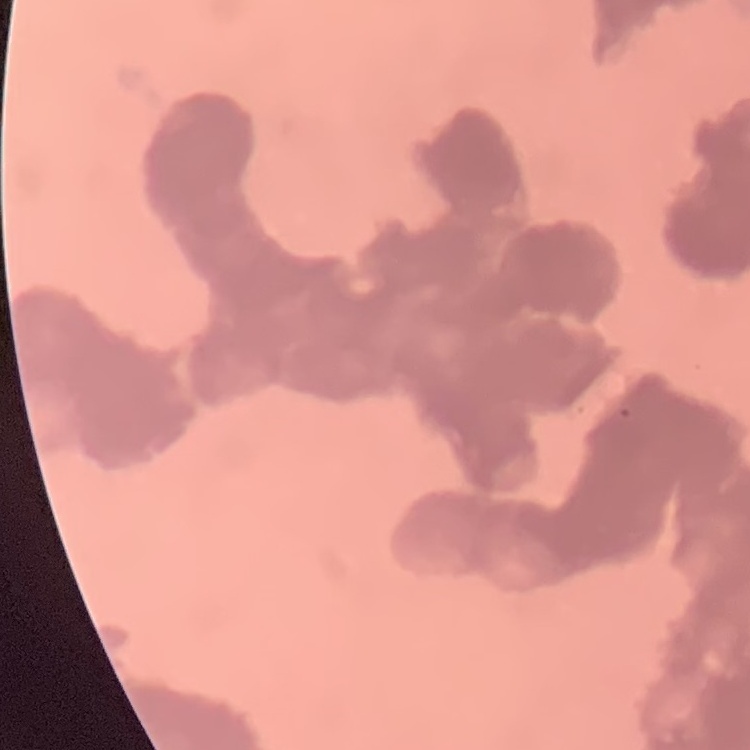

Summary:
  - Erythrocyte morphology: rouleaux formation
  - Image type: square crop of a larger photomicrograph
  - Stain: Field's or Giemsa
  - Preparation: thin blood film